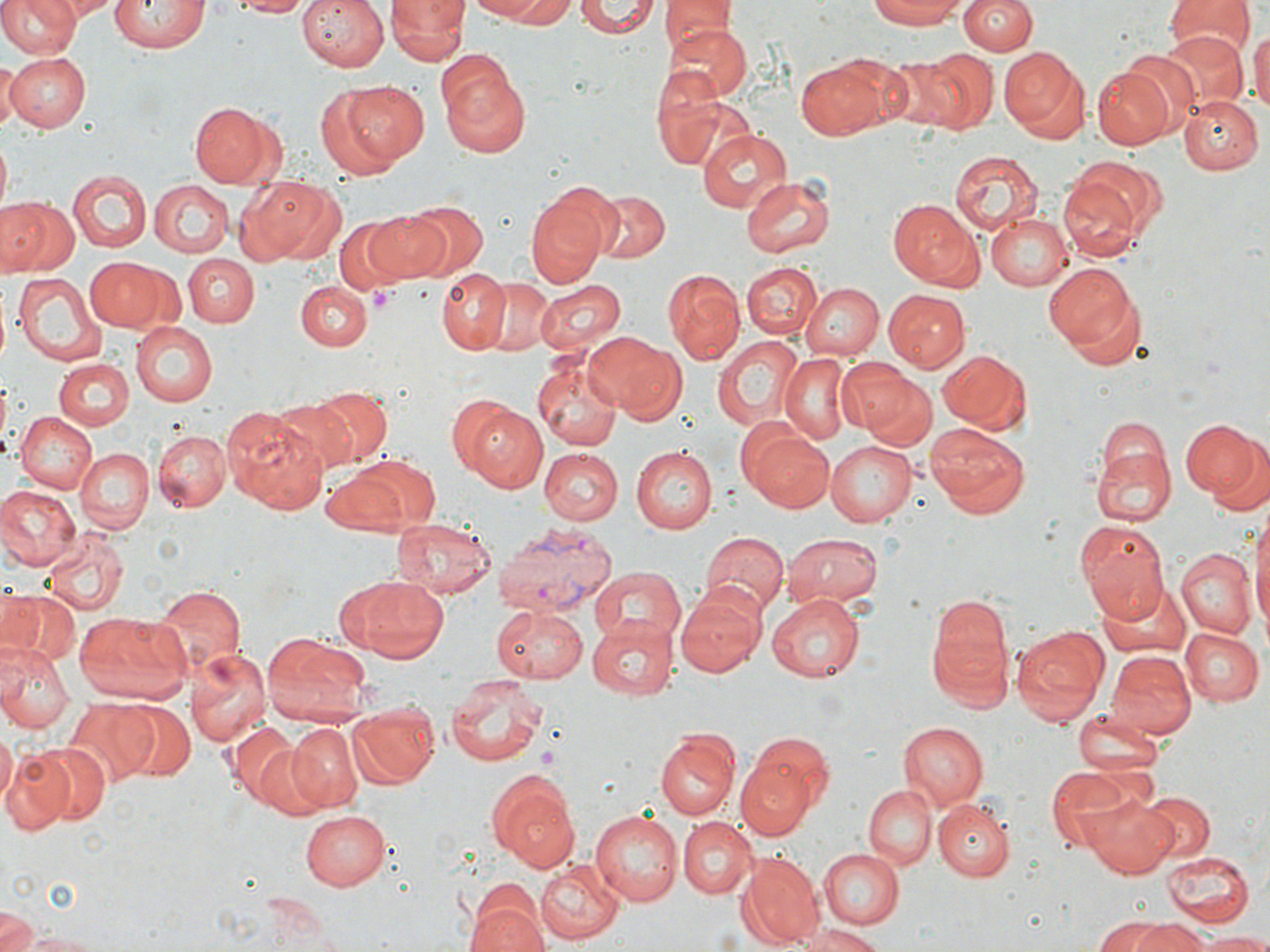
slide-level diagnosis = Plasmodium vivax
preparation = thin blood film
image size = 1270×952 pixels
stain = May-Grünwald-Giemsa
magnification = 1000x
uninfected red blood cell locations = approximate bounding boxes as (x1, y1, x2, y2) in pixels: (0, 0, 80, 58), (47, 0, 116, 20), (109, 0, 208, 54), (229, 0, 315, 17), (296, 0, 389, 73), (470, 0, 562, 23), (575, 0, 660, 39), (660, 0, 730, 48), (866, 0, 971, 29), (960, 0, 1035, 55), (386, 1, 466, 63), (1163, 1, 1254, 57), (661, 20, 750, 102), (1248, 26, 1270, 121), (1155, 27, 1252, 116), (999, 46, 1090, 139), (918, 48, 1000, 134), (6, 51, 91, 131), (436, 54, 531, 155), (861, 56, 965, 131), (797, 57, 892, 140), (0, 58, 18, 133), (1092, 63, 1179, 149), (651, 72, 729, 169), (340, 80, 431, 165), (314, 85, 400, 179), (1180, 92, 1263, 174), (189, 101, 284, 185), (696, 126, 791, 212), (712, 136, 824, 243), (950, 150, 1043, 235), (68, 170, 150, 252), (740, 174, 836, 261), (1060, 175, 1144, 262), (242, 177, 348, 265), (149, 180, 232, 256), (0, 184, 141, 268), (584, 185, 670, 266), (524, 187, 613, 288), (1, 196, 77, 276), (888, 198, 984, 292), (399, 201, 488, 279), (362, 210, 452, 282), (986, 211, 1072, 293), (333, 218, 414, 294), (180, 254, 256, 328), (86, 259, 164, 330), (742, 259, 823, 339), (1043, 262, 1138, 354), (435, 268, 509, 354), (663, 270, 746, 363), (12, 272, 105, 361), (483, 278, 556, 355), (533, 279, 626, 358), (803, 281, 884, 360), (295, 282, 370, 352), (883, 289, 971, 371), (132, 323, 218, 406), (583, 332, 677, 414), (710, 332, 803, 430), (936, 349, 1031, 435), (534, 355, 622, 452), (777, 356, 852, 445), (835, 357, 928, 441), (55, 358, 132, 432), (866, 378, 935, 452), (310, 387, 391, 462), (272, 396, 365, 475), (453, 399, 545, 491), (221, 408, 332, 512), (12, 411, 98, 495), (1178, 418, 1258, 500), (923, 423, 1031, 518), (742, 428, 835, 513), (154, 430, 231, 512), (1202, 433, 1270, 518), (824, 440, 916, 527), (630, 445, 717, 533), (1091, 445, 1175, 529), (75, 448, 153, 533), (539, 448, 622, 524), (332, 453, 442, 537), (0, 486, 80, 572), (1248, 513, 1270, 641), (388, 517, 497, 600), (1075, 518, 1171, 621), (44, 527, 130, 617), (701, 531, 787, 615), (783, 531, 883, 609), (1174, 551, 1254, 640), (590, 568, 685, 651), (340, 577, 449, 666), (1097, 581, 1195, 663), (676, 584, 768, 677), (153, 586, 243, 677), (0, 588, 81, 664), (767, 594, 865, 683), (926, 597, 1015, 712), (490, 604, 588, 681), (73, 610, 191, 706), (589, 617, 682, 696), (1009, 623, 1109, 729), (1178, 625, 1262, 706), (261, 634, 370, 727), (0, 642, 72, 733), (185, 648, 270, 749), (1104, 650, 1195, 741), (445, 675, 549, 766), (65, 698, 159, 784), (121, 702, 194, 780), (346, 704, 440, 788), (1072, 706, 1165, 781), (897, 721, 988, 810), (225, 723, 302, 807), (285, 725, 362, 810), (0, 726, 16, 812), (656, 731, 738, 819), (741, 731, 837, 815), (28, 742, 111, 827), (253, 742, 335, 822), (2, 747, 75, 833), (734, 755, 816, 838), (1047, 764, 1150, 857), (484, 769, 580, 870), (864, 786, 936, 868), (1082, 790, 1180, 876), (1139, 791, 1214, 863), (934, 799, 1014, 881), (301, 810, 389, 891), (589, 810, 684, 905), (678, 817, 757, 898), (818, 849, 904, 929), (1160, 850, 1254, 928), (737, 853, 823, 947), (535, 856, 623, 944), (464, 895, 548, 952), (0, 913, 40, 952), (1095, 916, 1171, 952), (1137, 918, 1208, 952), (793, 923, 885, 952), (7, 929, 111, 950), (1192, 931, 1270, 951)
field of view = one of a larger specimen
platelet locations = approximate bounding boxes as (x1, y1, x2, y2) in pixels: (370, 288, 393, 309)
Plasmodium vivax-infected red blood cell locations = approximate bounding boxes as (x1, y1, x2, y2) in pixels: (492, 523, 616, 615)
modality = optical microscopy